Comment on the morphology of the red blood cells.
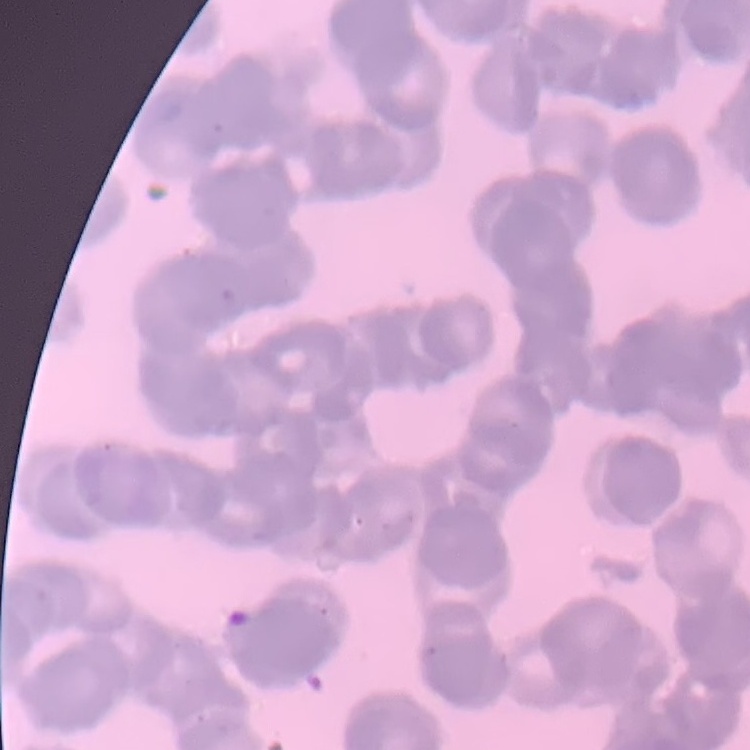
They show rouleaux formation.

{
  "image_type": "one tile cut from a larger photomicrograph",
  "preparation": "thin peripheral smear",
  "stain": "Field's or Giemsa"
}